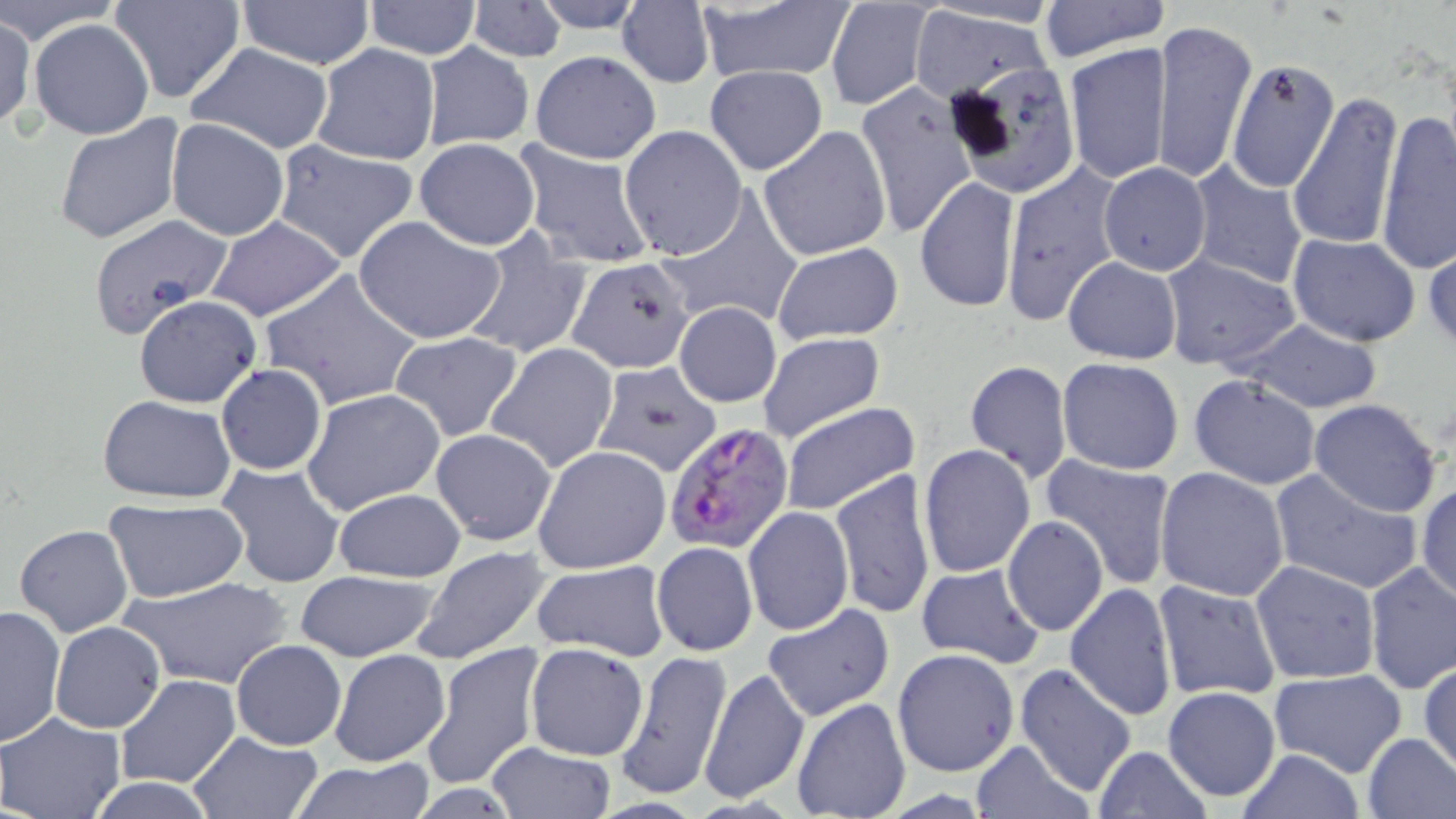

Approximate bounding boxes as (x1, y1, x2, y2) in pixels. Plasmodium falciparum-infected red blood cell locations: (664, 420, 795, 557). Uninfected red blood cell locations: (0, 0, 120, 42), (110, 0, 243, 104), (527, 0, 651, 33), (825, 0, 937, 112), (1037, 0, 1170, 61), (362, 1, 483, 58), (237, 2, 376, 69), (466, 2, 568, 62), (616, 2, 714, 87), (694, 2, 855, 83), (907, 5, 1058, 102), (0, 12, 35, 130), (1153, 17, 1257, 185), (29, 18, 155, 141), (420, 42, 535, 151), (1067, 42, 1170, 185), (187, 43, 335, 154), (310, 44, 440, 166), (531, 51, 660, 163), (1227, 57, 1340, 193), (705, 64, 827, 175), (855, 85, 977, 238), (1286, 88, 1404, 250), (1376, 106, 1455, 275), (54, 114, 186, 247), (165, 118, 289, 241), (620, 125, 748, 259), (759, 125, 891, 262), (414, 137, 541, 250), (273, 140, 418, 262), (513, 140, 657, 271), (1000, 161, 1125, 327), (1187, 161, 1308, 289), (1099, 162, 1211, 276), (915, 177, 1020, 314), (655, 189, 803, 329), (87, 206, 234, 329), (354, 216, 504, 345), (207, 217, 345, 320), (461, 231, 594, 361), (1288, 233, 1420, 346), (1425, 241, 1456, 352), (772, 243, 904, 347), (1160, 254, 1301, 371), (1061, 255, 1182, 364), (567, 257, 696, 375), (259, 268, 424, 412), (139, 298, 266, 410), (674, 302, 781, 407), (1231, 318, 1385, 416), (389, 331, 525, 443), (758, 332, 885, 443), (485, 342, 618, 473), (1057, 358, 1186, 475), (964, 359, 1073, 484), (590, 361, 723, 478), (216, 364, 326, 475), (1190, 375, 1320, 489), (302, 387, 446, 515), (98, 395, 236, 502), (1309, 399, 1443, 518), (780, 401, 919, 516), (431, 428, 558, 544), (533, 444, 672, 575), (918, 444, 1036, 580), (1038, 455, 1177, 590), (215, 463, 347, 588), (1155, 467, 1290, 602), (1269, 468, 1425, 595), (829, 470, 937, 621), (1416, 480, 1456, 605), (333, 487, 466, 583), (315, 491, 455, 660), (103, 499, 247, 603), (743, 507, 853, 636), (1002, 516, 1109, 635), (14, 524, 134, 637), (651, 541, 758, 655), (409, 544, 553, 663), (1251, 560, 1379, 683), (534, 561, 669, 659), (915, 562, 1046, 670), (1364, 562, 1456, 694), (294, 569, 441, 661), (120, 575, 294, 690), (1152, 580, 1282, 702), (1066, 582, 1178, 721), (1, 603, 66, 746), (764, 605, 893, 719), (49, 620, 166, 734), (230, 640, 345, 750), (421, 640, 547, 791), (525, 642, 649, 760), (616, 648, 732, 801), (891, 648, 1020, 777), (331, 649, 451, 766), (1421, 660, 1455, 776), (1015, 664, 1138, 797), (699, 666, 808, 805), (1269, 668, 1407, 776), (114, 674, 238, 789), (1162, 685, 1280, 800), (792, 697, 911, 819), (0, 711, 126, 819), (1361, 732, 1456, 818), (186, 733, 324, 817), (970, 738, 1093, 818), (484, 742, 617, 819), (1093, 745, 1210, 819), (1234, 748, 1366, 818), (285, 759, 437, 819). Slide-level diagnosis: Plasmodium falciparum. Image is 1456×819 pixels. Thin blood smear. Single field of view. May-Grünwald-Giemsa-stained preparation. 1000x magnification. Optical microscopy.